Classify this cell by malaria status.
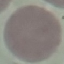

It is uninfected.

Thin blood film. Photographed with a smartphone camera at the microscope eyepiece. Automatically extracted cell patch, resized to 64 × 64 pixels. Giemsa stain.